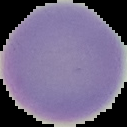

image_size: 127×127 pixels
result: negative for malaria parasites
preparation: thin blood film
image_type: segmented cell region with the area outside set to black